Report the malaria status of this cell.
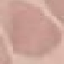

Uninfected.

Thin blood film. Acquired by smartphone through the microscope eyepiece. Cell patch, automatically extracted from a larger field of view and resized to 64 × 64 pixels. Giemsa stain.